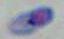

identification = Toxoplasma gondii
modality = photomicrograph
magnification = 1000x